Locate every malaria parasite.
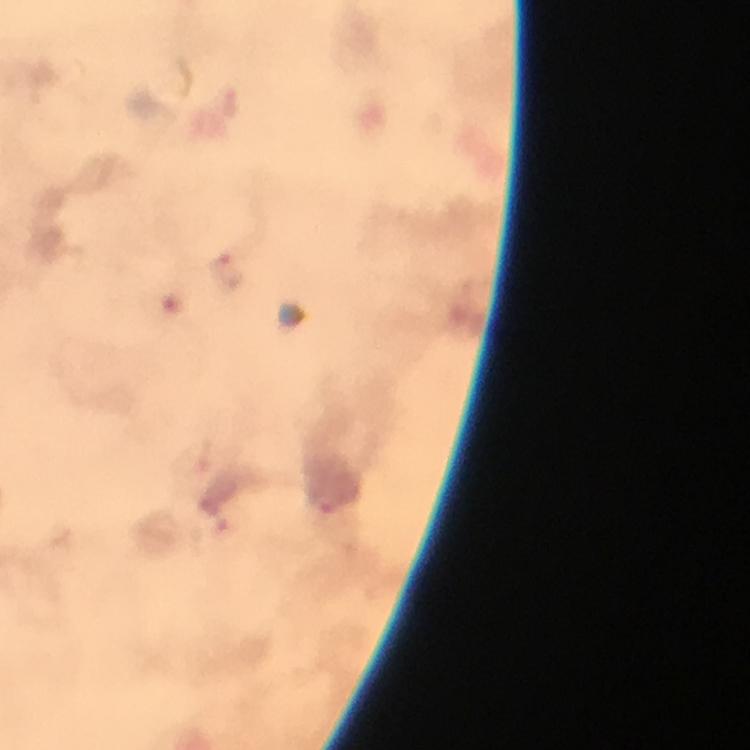

Approximate object centers, in pixels from the top-left corner.
Malaria parasites: (x=226, y=270).

Summary:
  - Magnification: 100x
  - Preparation: thick blood film
  - Immersion oil: applied
  - Stain: Giemsa
  - Image size: 750×750 pixels
  - Cropped from: one field of view
  - Capture: smartphone mounted on the microscope
  - Context: from a diagnostic examination for malaria